Locate platelets.
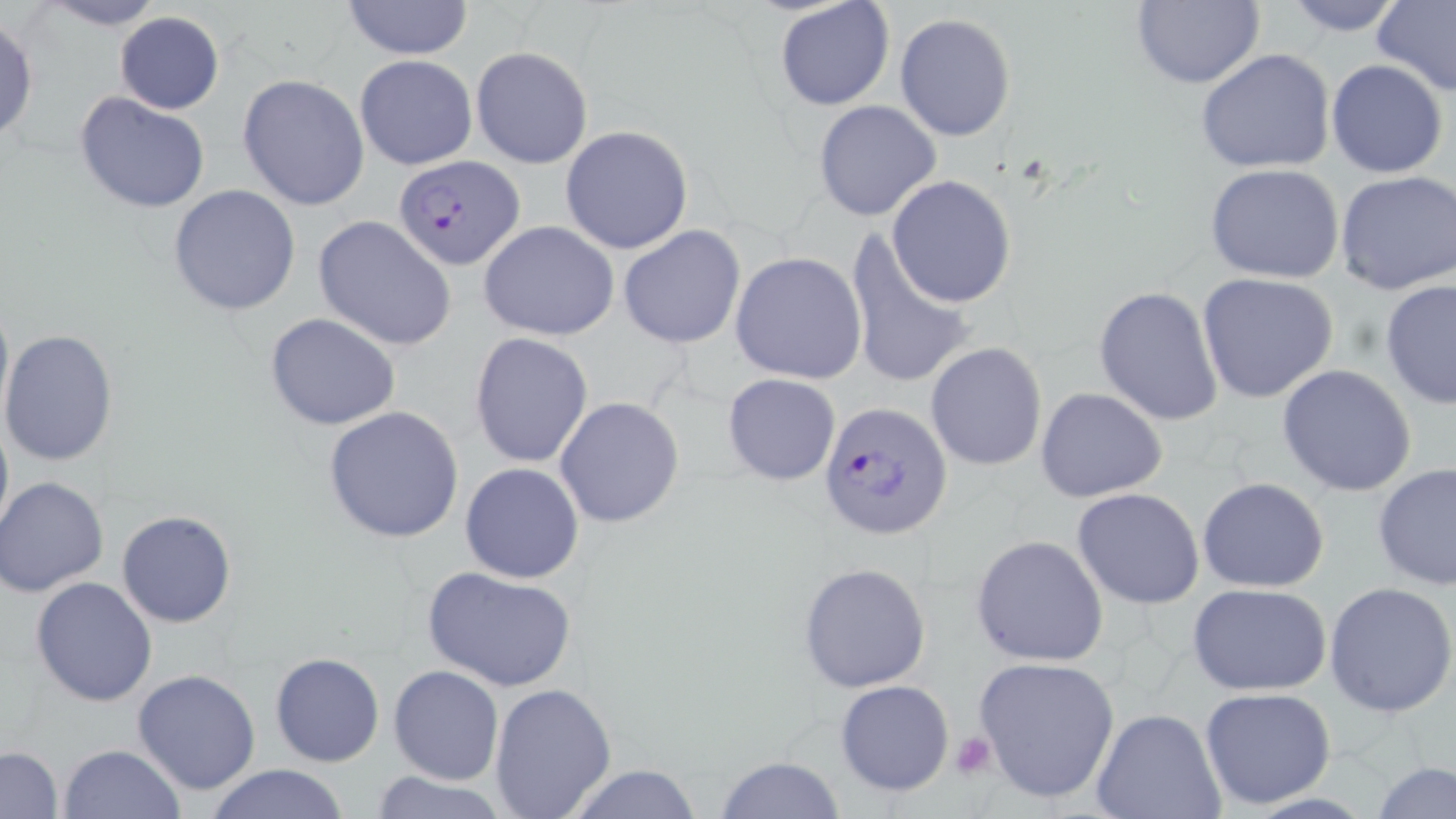
Approximate bounding boxes as (x1,y1)-(x2,y2) corner pairs in pixels.
Platelets: (948,732)-(997,780).

Uninfected red blood cell locations: (34,0)-(169,31), (339,0)-(475,59), (773,0)-(896,113), (1131,0)-(1264,90), (1376,0)-(1456,99), (1280,1)-(1411,36), (114,11)-(223,113), (895,14)-(1017,140), (0,15)-(39,145), (470,46)-(594,170), (1194,49)-(1337,174), (354,55)-(477,171), (1326,58)-(1448,178), (237,74)-(369,212), (74,90)-(211,215), (813,100)-(942,221), (559,125)-(694,254), (1203,164)-(1348,284), (1335,171)-(1456,297), (886,175)-(1017,307), (168,184)-(301,317), (314,215)-(458,353), (478,220)-(618,340), (619,226)-(747,348), (842,228)-(978,393), (730,252)-(867,384), (1196,271)-(1340,404), (1379,278)-(1456,412), (1094,286)-(1225,426), (0,288)-(12,427), (265,311)-(401,431), (1,329)-(119,468), (470,332)-(595,469), (925,342)-(1047,472), (1277,365)-(1417,496), (722,372)-(841,486), (1035,387)-(1169,502), (553,396)-(685,528), (0,405)-(12,544), (323,406)-(464,544), (460,462)-(584,584), (1372,463)-(1456,591), (0,476)-(110,598), (1196,477)-(1330,591), (1072,487)-(1204,609), (117,510)-(236,627), (971,533)-(1110,667), (797,560)-(933,693), (421,566)-(579,694), (31,576)-(159,706), (1188,583)-(1333,695), (1326,583)-(1456,719), (270,652)-(383,768), (973,654)-(1120,803), (388,665)-(504,784), (132,670)-(261,794), (834,679)-(955,796), (489,683)-(617,816), (1199,687)-(1337,810), (1090,709)-(1226,819), (59,743)-(184,819), (1,746)-(63,818), (715,754)-(845,819), (1373,760)-(1455,818), (202,762)-(353,819), (561,763)-(706,819), (365,769)-(512,819). Plasmodium falciparum-infected red blood cell locations: (393,156)-(523,271), (820,403)-(952,541). Slide-level diagnosis: Plasmodium falciparum. Image is 1456×819 pixels. 1000x magnification. Optical microscopy. One field of a larger specimen. May-Grünwald-Giemsa-stained preparation. Thin blood film.